Report the malaria status of this cell.
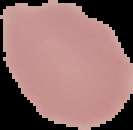

Uninfected.

Summary:
  - Image type: segmented cell region on a black background
  - Preparation: thin blood film
  - Image size: 133×130 pixels